Identify the cell.
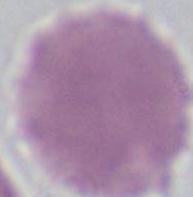

This is an erythrocyte.

magnification = 1000x
modality = micrograph